State which parasite is depicted.
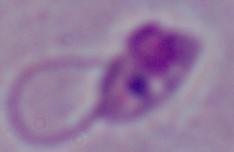

This is Leishmania.

Summary:
  - Modality: micrograph
  - Magnification: 1000x